Comment on the morphology of the red blood cells.
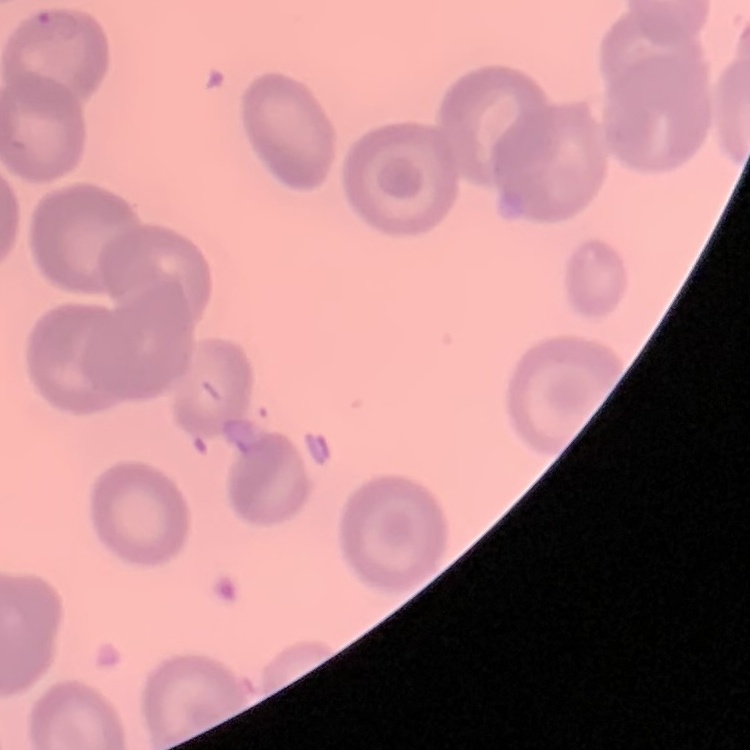
They show no rouleaux formation.

image type = one tile cut from a larger photomicrograph
stain = Field's or Giemsa
preparation = thin peripheral smear